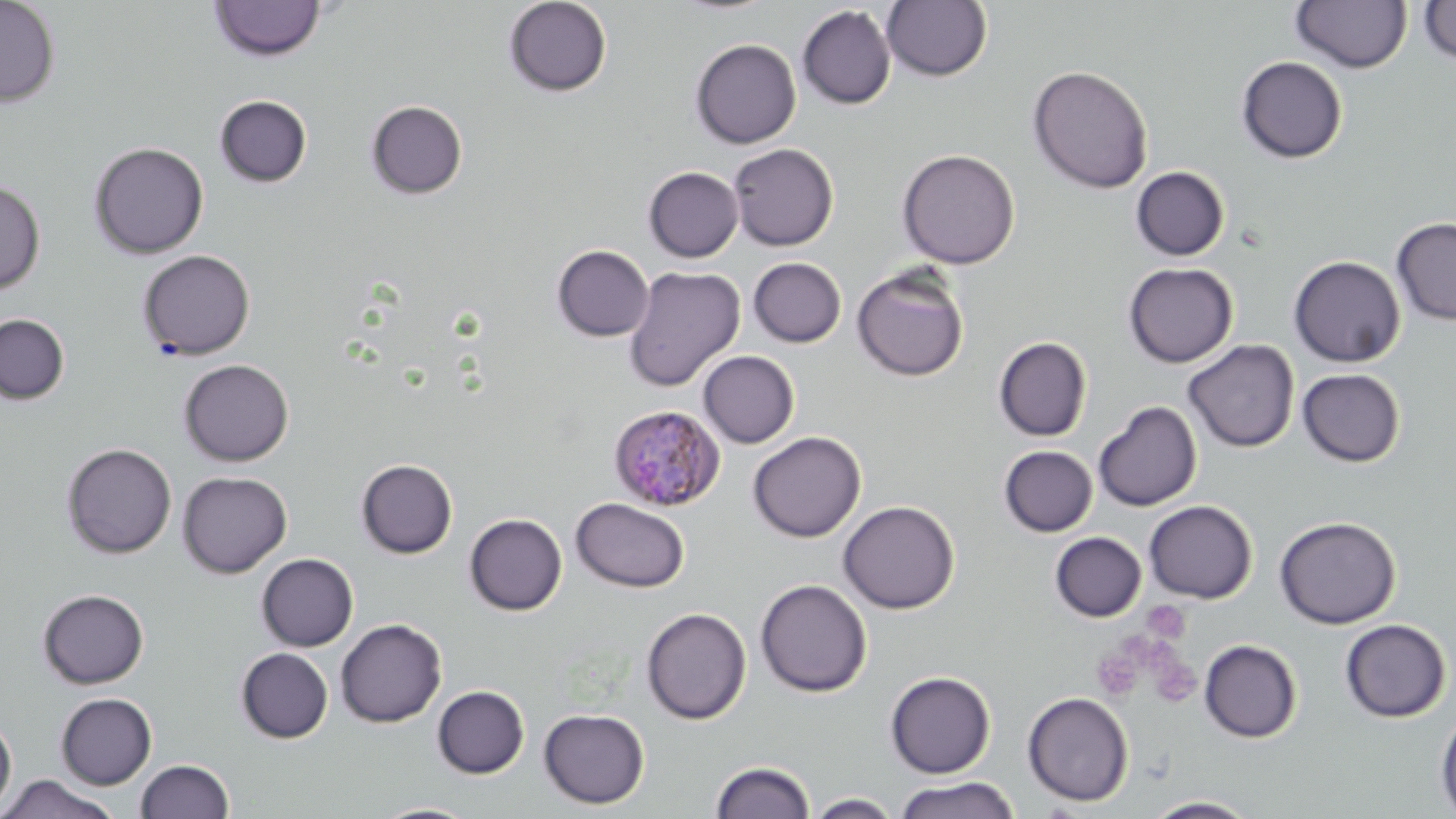
Approximate bounding boxes as named x1/y1/x2/y2 corners in pixels. Plasmodium malariae-infected red blood cell locations: (x1=607, y1=404, x2=726, y2=512). Platelet locations: (x1=1092, y1=646, x2=1145, y2=701). Uninfected red blood cell locations: (x1=0, y1=0, x2=61, y2=108), (x1=503, y1=0, x2=613, y2=97), (x1=209, y1=1, x2=327, y2=62), (x1=882, y1=1, x2=991, y2=82), (x1=1290, y1=1, x2=1413, y2=73), (x1=1418, y1=1, x2=1456, y2=64), (x1=797, y1=5, x2=896, y2=109), (x1=689, y1=38, x2=801, y2=149), (x1=1236, y1=56, x2=1348, y2=163), (x1=1027, y1=65, x2=1153, y2=193), (x1=214, y1=95, x2=312, y2=187), (x1=366, y1=100, x2=468, y2=199), (x1=89, y1=141, x2=209, y2=259), (x1=728, y1=143, x2=838, y2=251), (x1=897, y1=148, x2=1020, y2=270), (x1=1130, y1=166, x2=1229, y2=261), (x1=643, y1=167, x2=744, y2=262), (x1=0, y1=179, x2=45, y2=294), (x1=1391, y1=217, x2=1456, y2=325), (x1=552, y1=245, x2=654, y2=341), (x1=137, y1=249, x2=255, y2=360), (x1=1288, y1=255, x2=1406, y2=368), (x1=747, y1=257, x2=846, y2=347), (x1=1122, y1=262, x2=1238, y2=368), (x1=851, y1=264, x2=969, y2=382), (x1=623, y1=266, x2=745, y2=392), (x1=0, y1=314, x2=69, y2=404), (x1=993, y1=337, x2=1092, y2=441), (x1=1183, y1=339, x2=1300, y2=453), (x1=699, y1=351, x2=800, y2=448), (x1=178, y1=359, x2=293, y2=466), (x1=1297, y1=368, x2=1406, y2=467), (x1=1093, y1=401, x2=1202, y2=511), (x1=748, y1=431, x2=866, y2=542), (x1=61, y1=442, x2=177, y2=559), (x1=998, y1=445, x2=1098, y2=537), (x1=356, y1=459, x2=457, y2=559), (x1=177, y1=471, x2=292, y2=578), (x1=572, y1=498, x2=689, y2=592), (x1=837, y1=500, x2=960, y2=614), (x1=1143, y1=500, x2=1258, y2=603), (x1=464, y1=513, x2=567, y2=615), (x1=1274, y1=515, x2=1401, y2=629), (x1=1050, y1=532, x2=1147, y2=622), (x1=256, y1=553, x2=359, y2=651), (x1=755, y1=579, x2=873, y2=698), (x1=37, y1=589, x2=149, y2=689), (x1=641, y1=607, x2=751, y2=724), (x1=335, y1=618, x2=447, y2=727), (x1=1339, y1=619, x2=1452, y2=722), (x1=1199, y1=639, x2=1302, y2=743), (x1=236, y1=647, x2=333, y2=743), (x1=885, y1=670, x2=996, y2=778), (x1=432, y1=685, x2=529, y2=778), (x1=1022, y1=691, x2=1134, y2=806), (x1=56, y1=693, x2=156, y2=789), (x1=539, y1=708, x2=650, y2=809), (x1=1435, y1=708, x2=1456, y2=816), (x1=0, y1=715, x2=16, y2=814), (x1=135, y1=759, x2=235, y2=819), (x1=710, y1=760, x2=816, y2=819), (x1=1, y1=774, x2=120, y2=819), (x1=894, y1=777, x2=1020, y2=819), (x1=807, y1=793, x2=901, y2=818), (x1=1141, y1=795, x2=1259, y2=818), (x1=371, y1=802, x2=481, y2=819). Slide-level diagnosis: Plasmodium malariae. Thin blood film. May-Grünwald-Giemsa stain. Captured at 1000x magnification. Image is 1456×819 pixels. Single field of view. Optical microscopy.